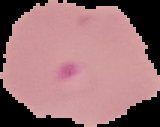

{
  "image_size": "160×127 pixels",
  "image_type": "segmented cell region on a black background",
  "preparation": "thin blood film",
  "malaria_status": "parasitized"
}